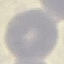
Summary:
  - Malaria status: uninfected
  - Capture: smartphone through the microscope eyepiece
  - Image type: automatically extracted cell patch, resized to 64 × 64 pixels
  - Preparation: thin blood smear
  - Stain: Giemsa